Name the cell type shown.
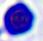
A leukocyte.

modality = photomicrograph
magnification = 400x